Locate every leukocyte (white blood cell).
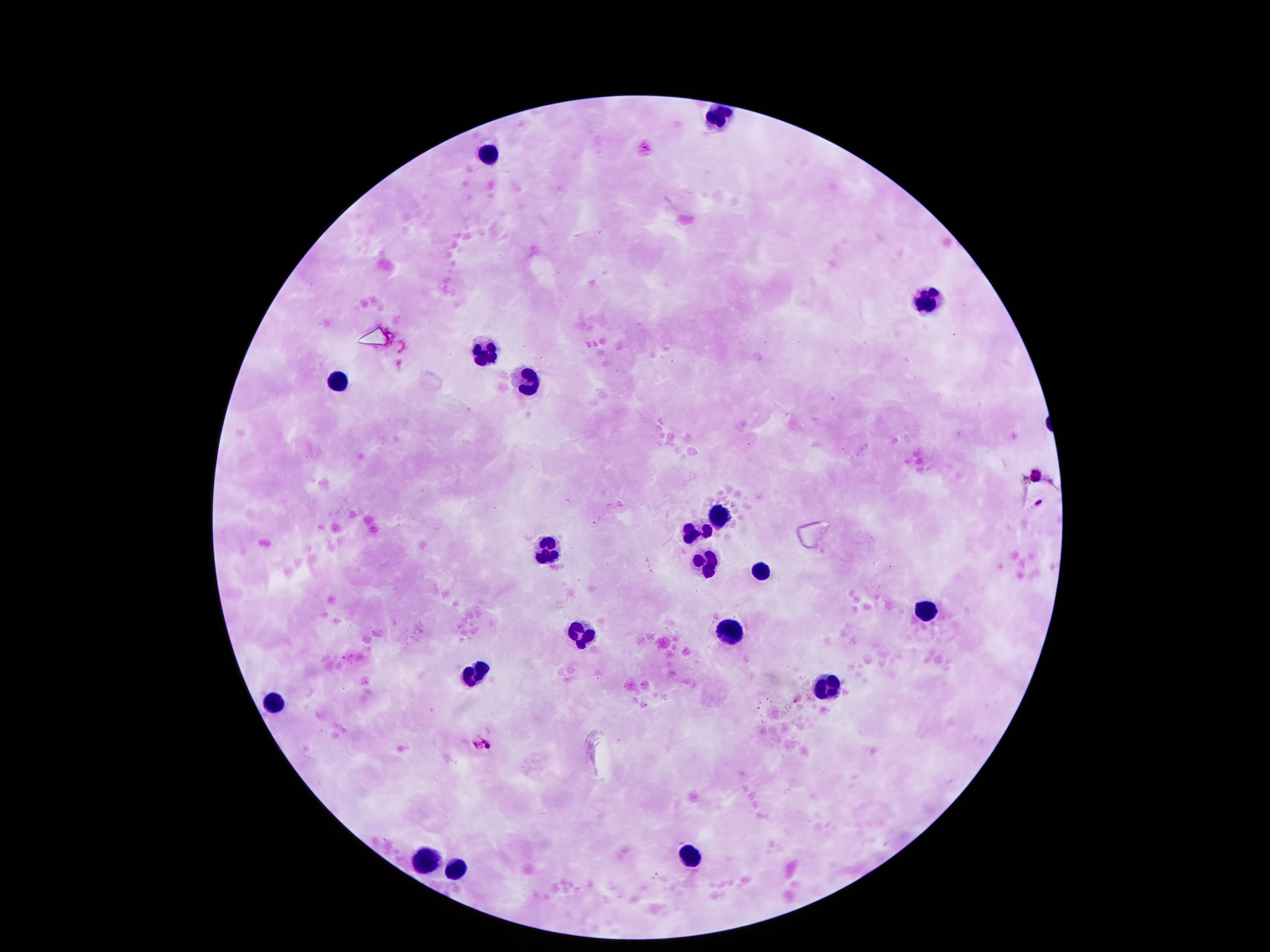
Approximate object centers, in pixels from the top-left corner.
Leukocytes: (x=489, y=156), (x=929, y=301), (x=483, y=347), (x=525, y=378), (x=337, y=382), (x=722, y=518), (x=696, y=533), (x=547, y=549), (x=706, y=559), (x=761, y=566), (x=932, y=605), (x=735, y=628), (x=580, y=631), (x=473, y=672), (x=828, y=683), (x=273, y=702), (x=689, y=851), (x=424, y=857), (x=454, y=864).

capture = smartphone camera through the microscope eyepiece
magnification = 100x
image size = 1270×952 pixels
patient malaria status = negative
field of view = one from this slide
preparation = thick blood smear
stain = Giemsa